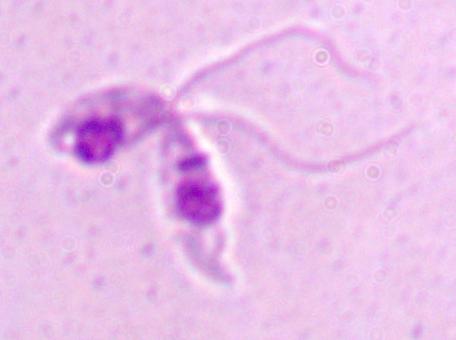

A Leishmania parasite is seen. Captured at 1000x magnification. Micrograph.